State which parasite is depicted.
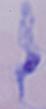

A trypanosome.

Summary:
  - Magnification: 1000x
  - Modality: photomicrograph